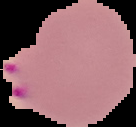
image size = 136×127 pixels
preparation = thin blood smear
image type = segmented cell region on a black background
result = Plasmodium parasites detected